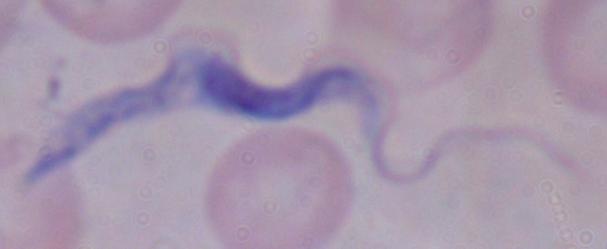

Summary:
  - Modality: photomicrograph
  - Magnification: 1000x
  - Identification: trypanosome